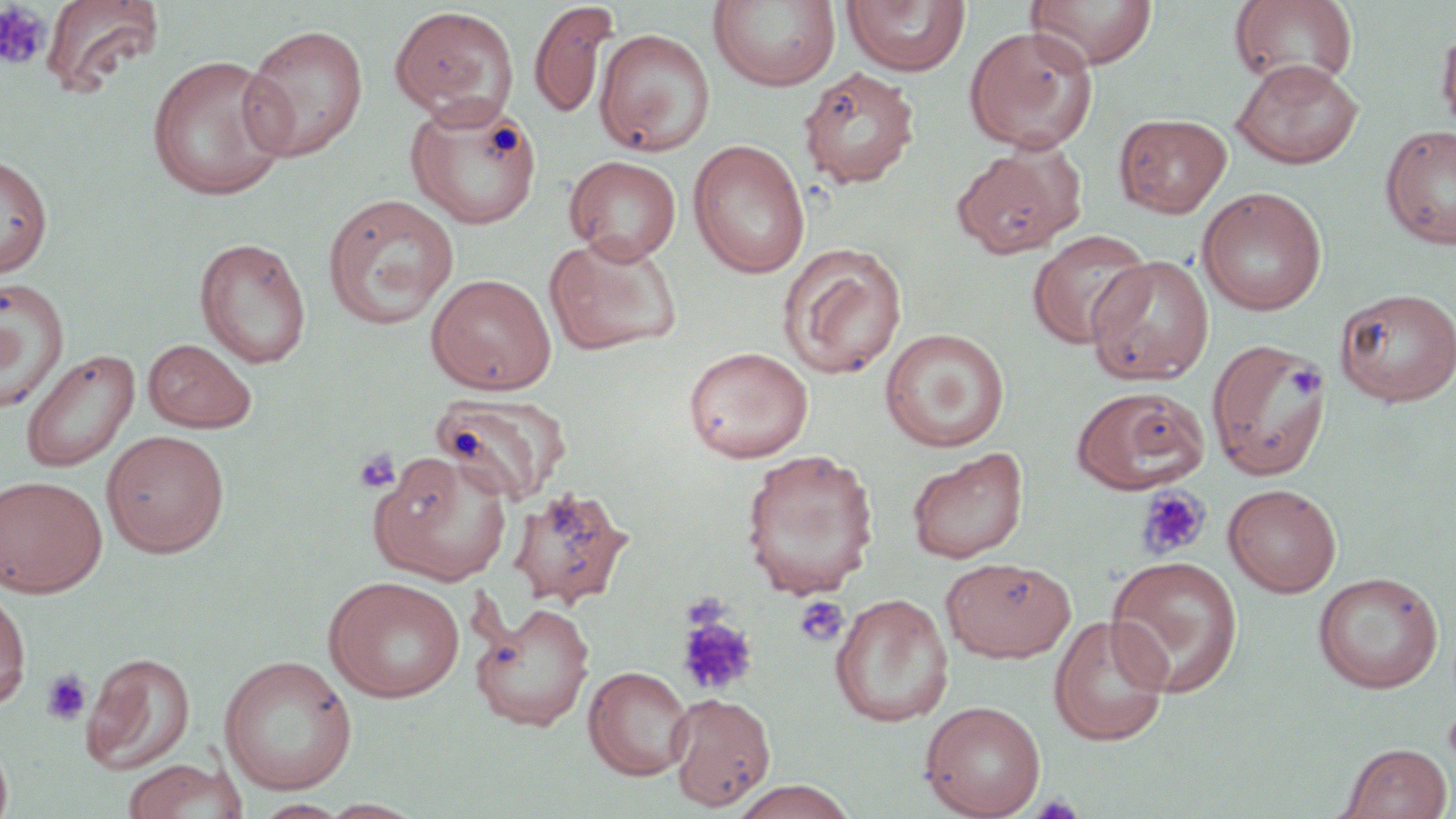

Summary:
  - Coordinate format: approximate bounding boxes as (x1,y1)-(x2,y2) corner pairs in pixels
  - Uninfected red blood cell locations: (40,0)-(164,99), (708,0)-(841,92), (1025,0)-(1158,69), (1230,0)-(1359,90), (528,2)-(619,121), (841,2)-(971,77), (390,5)-(519,125), (1436,18)-(1456,140), (240,23)-(369,162), (964,25)-(1098,152), (594,28)-(715,157), (146,53)-(291,201), (1231,59)-(1363,168), (799,67)-(920,188), (406,99)-(544,232), (1114,112)-(1232,217), (1380,124)-(1456,250), (688,140)-(810,278), (962,140)-(1094,254), (0,153)-(53,280), (564,155)-(682,264), (1196,187)-(1328,315), (322,193)-(460,330), (1027,228)-(1153,349), (544,234)-(682,356), (194,236)-(311,368), (778,242)-(907,380), (1087,255)-(1214,384), (426,272)-(556,394), (0,277)-(70,413), (1334,287)-(1456,406), (880,328)-(1010,452), (143,338)-(257,433), (1207,338)-(1332,480), (683,346)-(813,463), (21,348)-(140,473), (1071,385)-(1209,493), (431,391)-(571,506), (100,429)-(230,558), (907,446)-(1029,564), (739,448)-(880,598), (369,450)-(513,585), (0,475)-(107,597), (1222,482)-(1342,596), (507,484)-(634,609), (1106,555)-(1244,697), (941,556)-(1076,662), (1313,571)-(1444,693), (324,576)-(466,703), (0,583)-(32,710), (831,593)-(953,728), (471,601)-(595,731), (1048,615)-(1172,746), (81,651)-(196,774), (218,654)-(358,795), (584,665)-(693,780), (667,692)-(776,811), (920,699)-(1046,817), (0,739)-(13,819), (1338,741)-(1454,819), (120,757)-(249,819), (726,780)-(861,819), (252,798)-(350,817), (319,799)-(425,818)
  - Platelet locations: (0,3)-(51,71), (1287,364)-(1325,400), (353,449)-(400,494), (1135,485)-(1210,561), (682,591)-(732,632), (794,596)-(849,647), (675,614)-(757,697), (41,669)-(92,726), (1442,708)-(1456,772)
  - Slide-level diagnosis: negative for blood parasites
  - Preparation: thin blood smear
  - Field of view: one of a larger specimen
  - Modality: optical microscopy
  - Magnification: 1000x
  - Stain: May-Grünwald-Giemsa
  - Image size: 1456×819 pixels